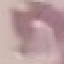

Result: no malaria parasites seen. Thin blood smear. Photographed with a smartphone camera at the microscope eyepiece. Cell patch, automatically extracted from a larger field of view and resized to 64 × 64 pixels. Giemsa-stained preparation.